Assess this cell for malaria.
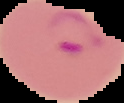

Parasitized.

From a thin blood film. Image is 124×103 pixels. Cell region segmented out of the field of view; the surrounding area is masked to black.